Comment on the morphology of the erythrocytes.
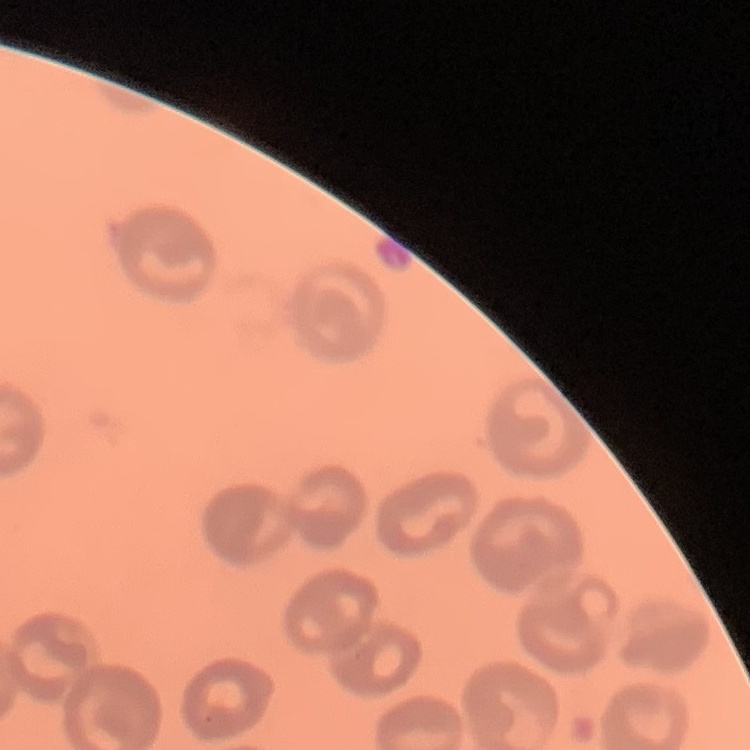

They show no rouleaux formation.

{
  "image_type": "square crop of a larger photomicrograph",
  "stain": "Field's or Giemsa",
  "preparation": "thin blood smear"
}